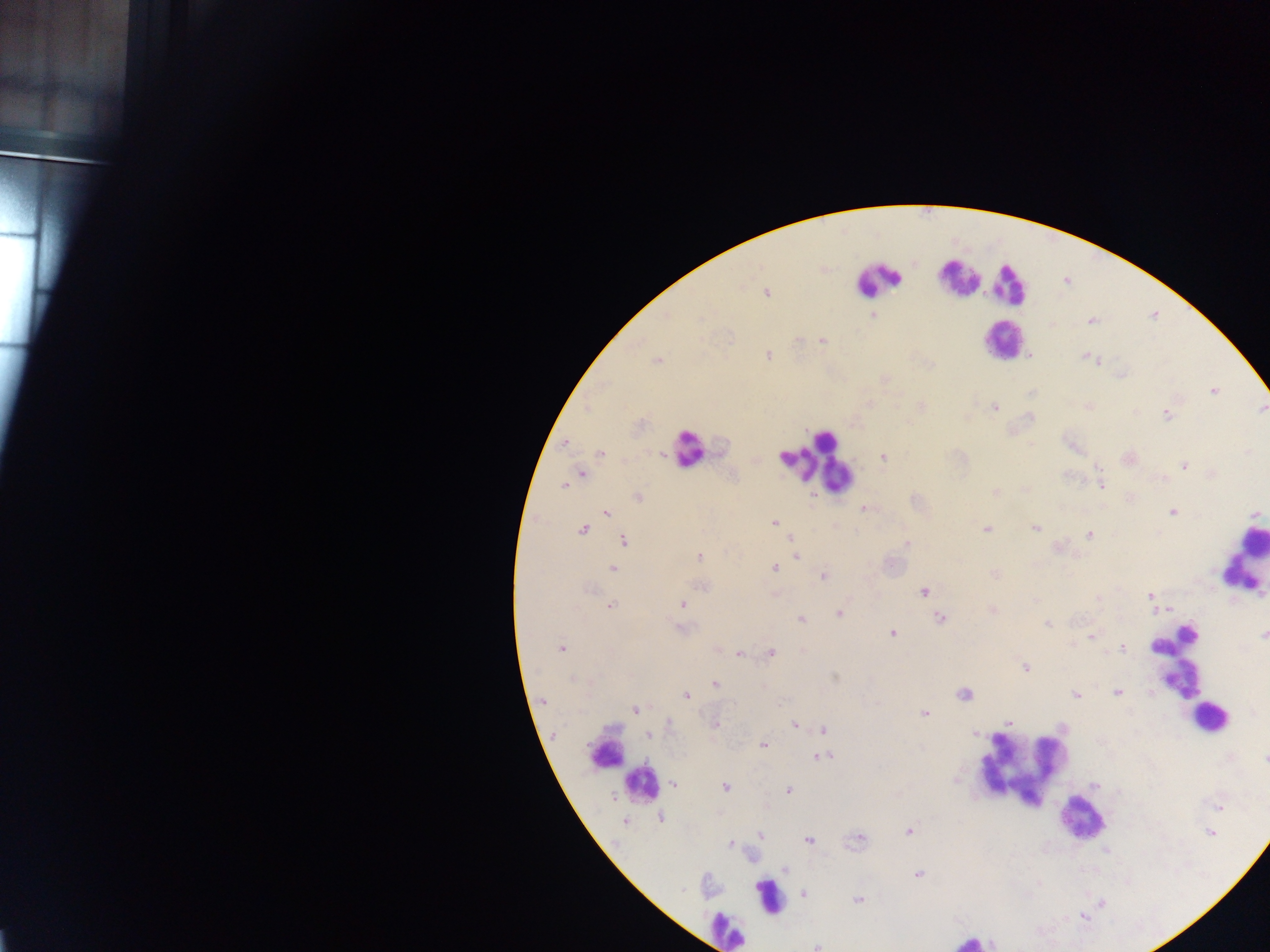

Approximate centers as {x, y} in pixels. Leukocyte locations: {958, 277}, {877, 280}, {1008, 284}, {1002, 340}, {687, 449}, {817, 464}, {1242, 561}, {1174, 661}, {1210, 717}, {607, 750}, {1023, 763}, {642, 785}, {1081, 818}, {768, 897}, {724, 930}, {971, 941}. Malaria parasite locations: {766, 292}, {873, 317}, {1091, 320}, {822, 339}, {766, 355}, {1030, 355}, {1084, 356}, {1091, 357}, {656, 360}, {1097, 360}, {1120, 375}, {884, 378}, {1213, 390}, {920, 406}, {993, 407}, {1089, 407}, {1262, 409}, {1166, 414}, {564, 442}, {600, 453}, {883, 457}, {1127, 457}, {1185, 465}, {580, 474}, {1100, 483}, {565, 484}, {995, 493}, {638, 497}, {1130, 498}, {864, 509}, {1172, 511}, {605, 512}, {1258, 514}, {773, 522}, {1034, 527}, {582, 528}, {986, 529}, {1090, 535}, {791, 538}, {623, 540}, {906, 543}, {795, 556}, {699, 557}, {613, 568}, {773, 568}, {995, 574}, {822, 576}, {701, 585}, {923, 590}, {774, 594}, {1150, 596}, {1098, 598}, {683, 604}, {610, 606}, {1170, 608}, {993, 610}, {838, 612}, {940, 618}, {799, 619}, {1047, 624}, {681, 628}, {892, 632}, {1263, 635}, {1091, 636}, {717, 647}, {1122, 647}, {561, 648}, {771, 652}, {739, 653}, {1026, 667}, {835, 677}, {715, 685}, {1117, 692}, {964, 693}, {1075, 694}, {686, 695}, {542, 702}, {635, 709}, {924, 713}, {1009, 722}, {715, 723}, {668, 724}, {794, 724}, {824, 730}, {647, 734}, {975, 734}, {763, 744}, {820, 756}, {1264, 759}, {674, 783}, {724, 787}, {788, 790}, {1218, 806}, {661, 817}, {624, 821}, {908, 830}, {1210, 831}, {760, 834}, {858, 837}, {808, 840}, {731, 844}, {784, 869}, {918, 874}, {804, 893}, {858, 899}, {1083, 915}, {817, 945}. Single field of view. Image is 1270×952 pixels. Sample from Ghana. Photographed through a microscope with a mobile-phone camera. Thick blood film.